Locate the red blood cells and classify each one as Plasmodium falciparum-infected, uninfected, or of indeterminate infection status.
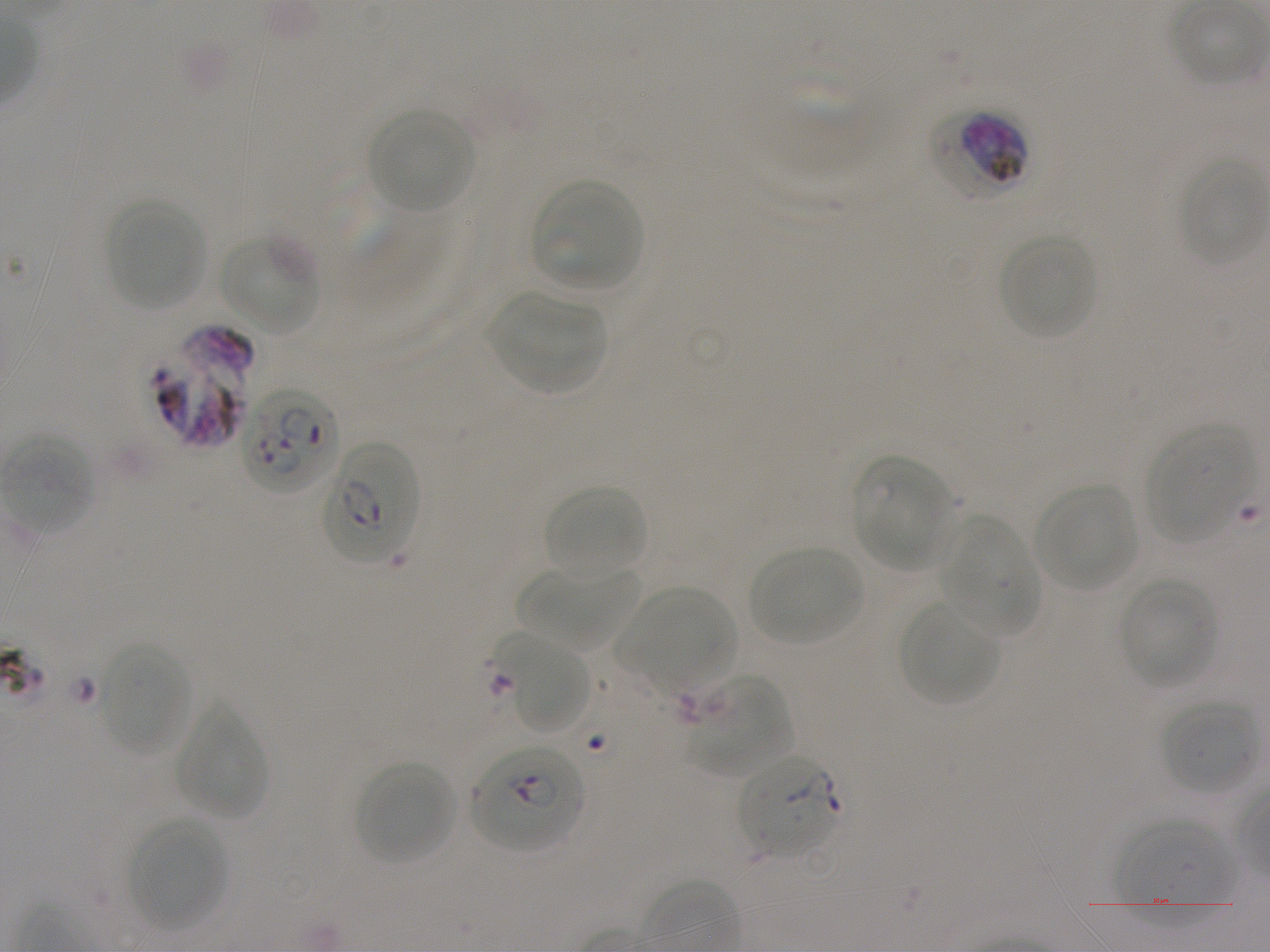

Approximate bounding rectangles given as corner coordinates in pixels from the top-left. Not every red blood cell is marked. A life-cycle stage — or a range of stages, where the recorded stages span more than one — follows each staged infected red blood cell.
Infected red blood cells: (x1=933, y1=108, x2=1028, y2=203) late trophozoite to late schizont; (x1=151, y1=326, x2=254, y2=449); (x1=239, y1=390, x2=338, y2=495); (x1=323, y1=443, x2=421, y2=566); (x1=471, y1=744, x2=585, y2=852) early ring to early trophozoite; (x1=737, y1=753, x2=841, y2=859) early ring to early trophozoite.
Uninfected red blood cells: (x1=369, y1=109, x2=474, y2=213), (x1=1182, y1=160, x2=1268, y2=268), (x1=531, y1=179, x2=643, y2=292), (x1=105, y1=199, x2=208, y2=311), (x1=999, y1=234, x2=1097, y2=340), (x1=219, y1=236, x2=319, y2=335), (x1=490, y1=291, x2=608, y2=393), (x1=1146, y1=425, x2=1258, y2=544), (x1=5, y1=435, x2=94, y2=535), (x1=850, y1=456, x2=953, y2=569), (x1=1034, y1=483, x2=1139, y2=592), (x1=544, y1=485, x2=647, y2=579), (x1=937, y1=514, x2=1038, y2=638), (x1=748, y1=546, x2=864, y2=647), (x1=518, y1=566, x2=637, y2=652), (x1=1117, y1=576, x2=1221, y2=689), (x1=613, y1=587, x2=736, y2=697), (x1=898, y1=598, x2=1001, y2=708), (x1=493, y1=629, x2=591, y2=735), (x1=99, y1=641, x2=191, y2=756), (x1=683, y1=673, x2=792, y2=777), (x1=1161, y1=698, x2=1259, y2=794), (x1=174, y1=705, x2=268, y2=820), (x1=354, y1=760, x2=459, y2=866), (x1=1115, y1=816, x2=1236, y2=926), (x1=127, y1=817, x2=229, y2=931).
No red blood cells of indeterminate infection status observed.

Image is 1270×952 pixels. Giemsa stain. One field from this slide. Thin blood smear. Blood group of the donor: A+. Static in-vitro culture of Plasmodium falciparum strain NF54. 100x oil-immersion objective, numerical aperture 1.25.